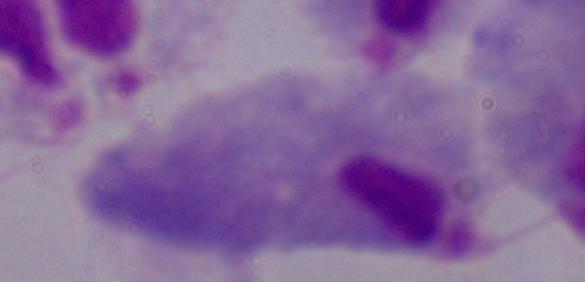

A trichomonad is seen. Captured at 1000x magnification. Photomicrograph.